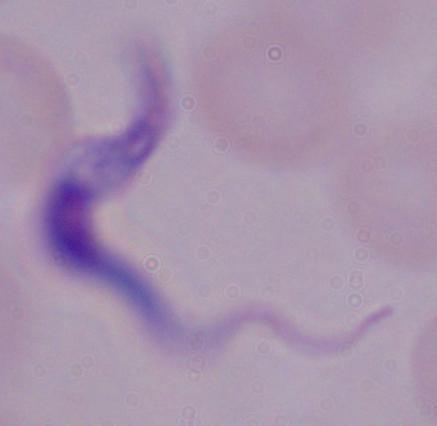
identification = trypanosome
magnification = 1000x
modality = micrograph